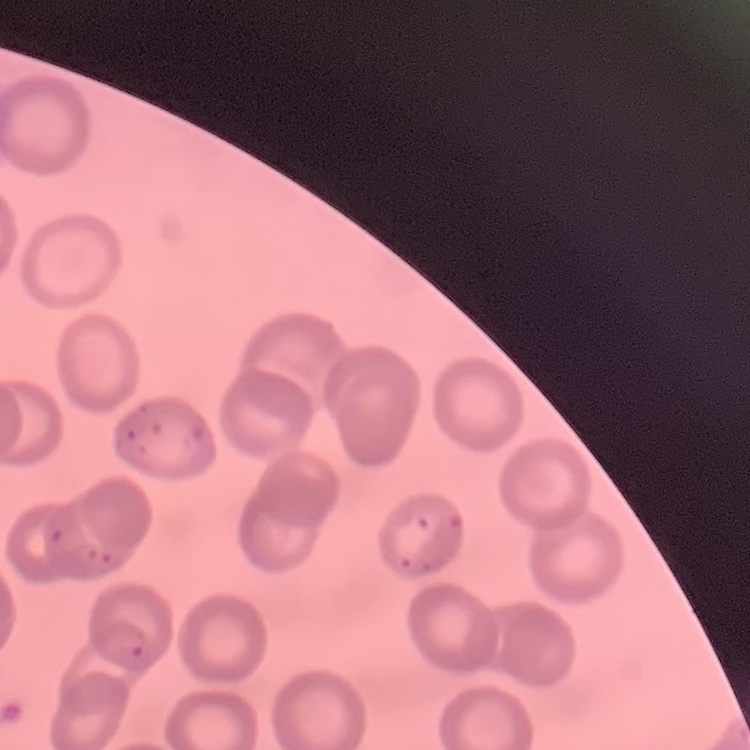
The red blood cells show no rouleaux formation. Square crop of a larger photomicrograph. Thin blood film. Stained with either Field's or Giemsa.